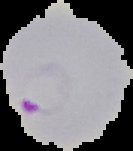
image type = segmented cell region with the area outside set to black
image size = 133×151 pixels
preparation = thin blood film
result = Plasmodium parasites detected